Comment on the morphology of the erythrocytes.
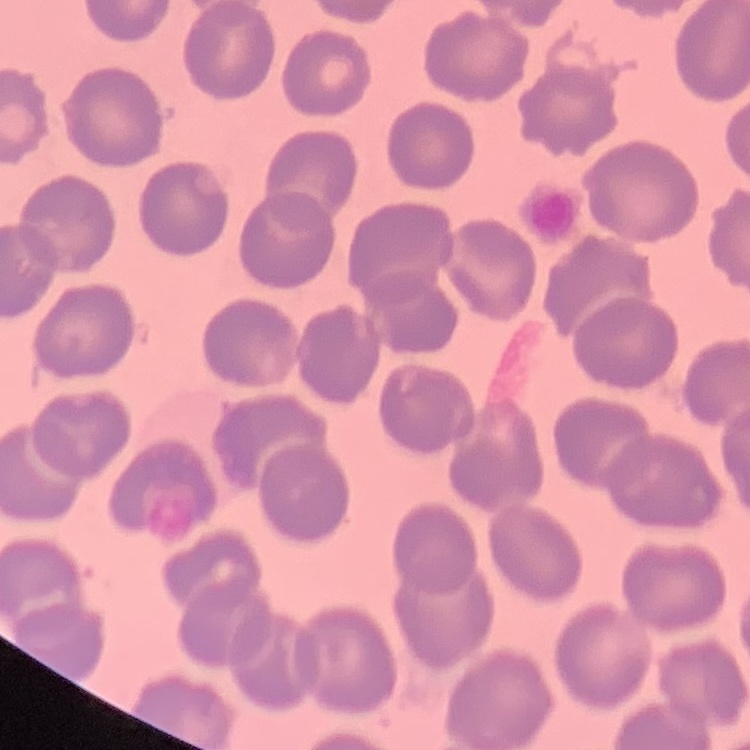
They show no rouleaux formation.

stain: Field's or Giemsa
image_type: square crop of a larger photomicrograph
preparation: thin blood smear